State which parasite is depicted.
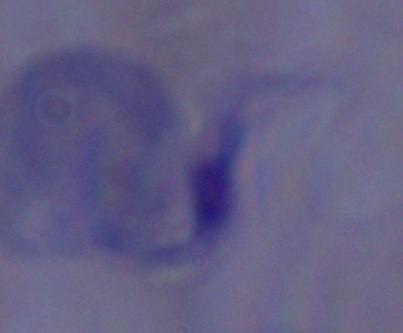
A trypanosome.

Summary:
  - Magnification: 1000x
  - Modality: micrograph